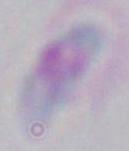
Summary:
  - Magnification: 1000x
  - Modality: micrograph
  - Identification: Toxoplasma gondii